Assess this cell for malaria.
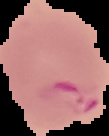

Parasitized.

Summary:
  - Preparation: thin blood film
  - Image type: segmented cell region on a black background
  - Image size: 109×136 pixels